Point out each malaria parasite.
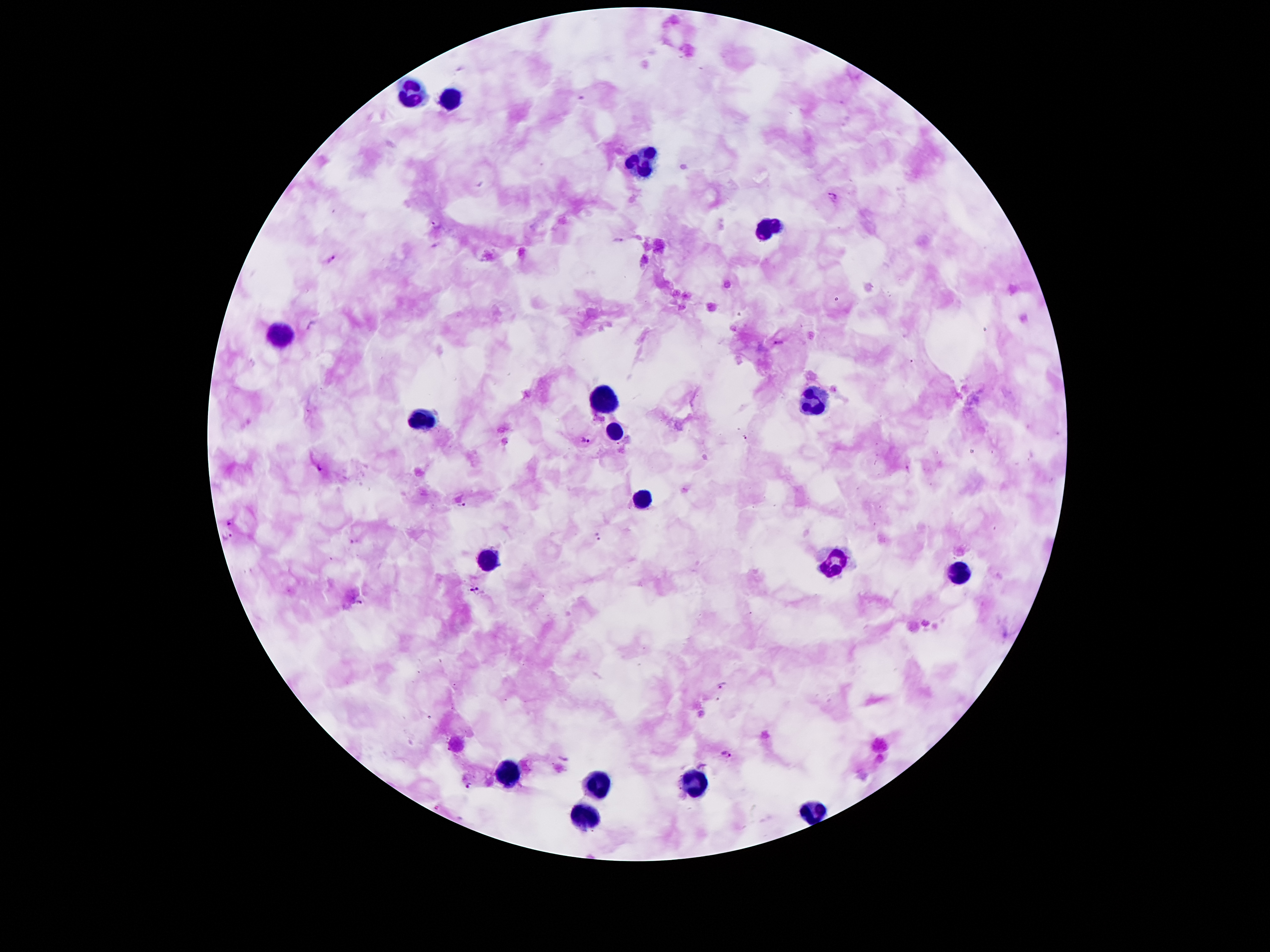
Approximate centers as [x, y] in pixels.
Malaria parasites: [834, 196], [437, 224], [618, 241], [331, 258], [779, 342], [745, 437], [585, 439], [317, 468], [462, 504], [230, 522], [598, 536], [227, 537], [474, 590], [361, 601], [722, 684], [726, 754], [469, 785].

Summary:
  - Leukocyte locations: [413, 90], [449, 97], [645, 160], [767, 228], [281, 331], [817, 396], [601, 398], [421, 418], [617, 431], [641, 498], [489, 556], [835, 565], [957, 571], [509, 771], [699, 779], [599, 781], [813, 812], [585, 814]
  - Patient malaria status: infected with Plasmodium falciparum
  - Image size: 1270×952 pixels
  - Stain: Giemsa
  - Preparation: thick peripheral-blood smear
  - Field of view: single
  - Capture: smartphone camera through the microscope eyepiece
  - Magnification: 100x